Name the cell type shown.
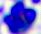

A leukocyte.

modality: photomicrograph
magnification: 400x